Assess this cell for malaria.
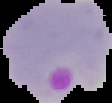

Parasitized.

Cell region segmented out of the field of view; the surrounding area is masked to black. From a thin blood film. Image is 112×103 pixels.